Report the malaria status of this cell.
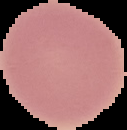
It is uninfected.

Summary:
  - Image type: segmented cell region on a black background
  - Preparation: thin blood smear
  - Image size: 127×130 pixels